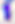 Toxoplasma gondii is shown. 400x magnification. Photomicrograph.